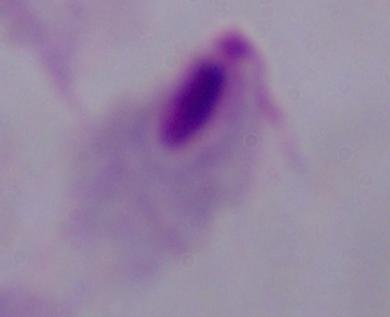
A trichomonad is seen. Captured at 1000x magnification. Photomicrograph.